Assess the morphology of the red blood cells.
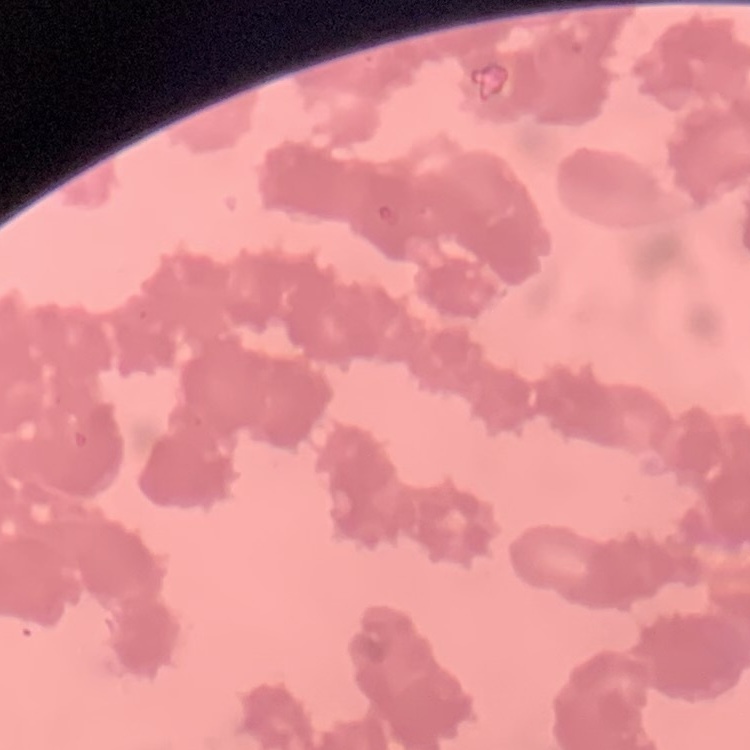
They show rouleaux formation.

Thin peripheral smear. Stained with either Field's or Giemsa. Square crop of a larger photomicrograph.